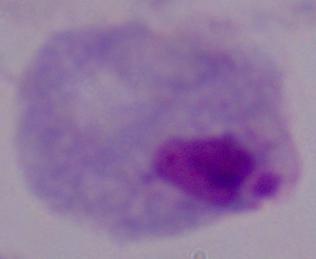

identification = trichomonad
magnification = 1000x
modality = photomicrograph